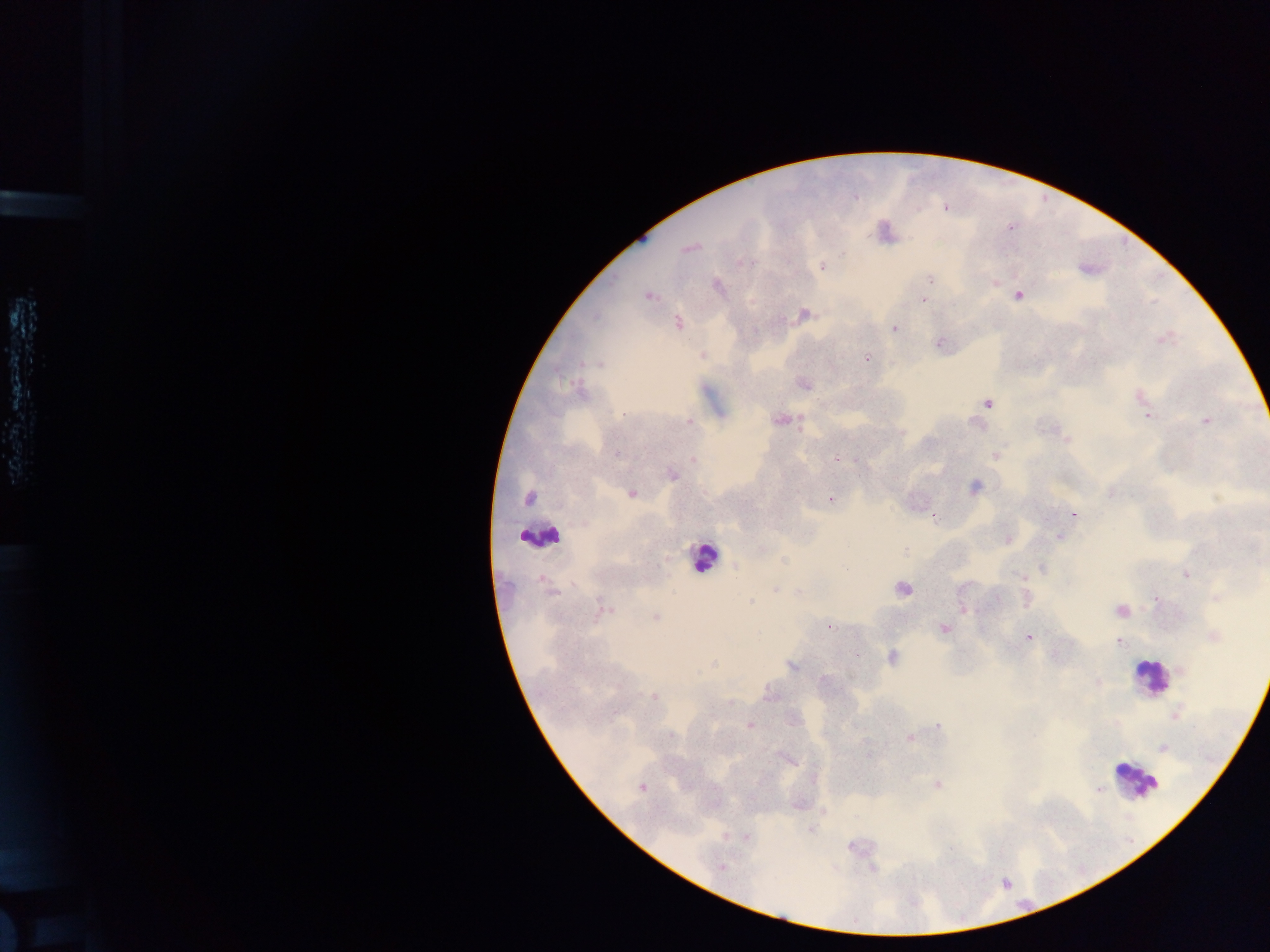
capture = mobile-phone photograph through a microscope
preparation = thick blood smear
country = Ghana
leukocyte locations = approximate centers as x y in pixels: 545 537; 703 560; 1151 681; 1140 780
Plasmodium parasite locations = approximate centers as x y in pixels: 688 249; 694 249; 843 254; 744 263; 821 266; 929 278; 993 282; 717 285; 648 295; 1018 295; 923 299; 804 314; 679 322; 892 328; 1164 338; 1160 341; 939 345; 703 355; 867 358; 582 363; 592 363; 599 364; 566 382; 575 385; 804 385; 583 388; 1136 396; 987 403; 1144 411; 622 414; 1147 416; 799 417; 777 420; 1205 421; 688 423; 800 426; 1068 440; 616 454; 995 455; 836 458; 693 461; 863 462; 672 475; 975 486; 632 495; 1215 497; 528 498; 830 498; 1073 513; 932 518; 1058 535; 1007 540; 906 550; 783 561; 1042 568; 1184 575; 1022 577; 543 581; 903 590; 774 591; 798 591; 553 592; 1214 598; 750 599; 600 604; 605 608; 963 610; 1121 611; 656 616; 830 627; 944 629; 1214 636; 1028 638; 1119 642; 858 655; 894 656; 713 663; 791 666; 851 675; 825 679; 1098 680; 655 696; 730 703; 1175 717; 749 725; 939 726; 909 738; 793 761; 938 785; 642 788; 1100 790; 811 831; 726 835; 745 837; 950 849; 721 869
image size = 1270×952 pixels
field of view = single